Report the malaria status of this cell.
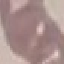

It is uninfected.

Summary:
  - Stain: Giemsa
  - Preparation: thin blood smear
  - Capture: smartphone through the microscope eyepiece
  - Image type: cell patch, automatically extracted from a larger field of view and resized to 64 × 64 pixels